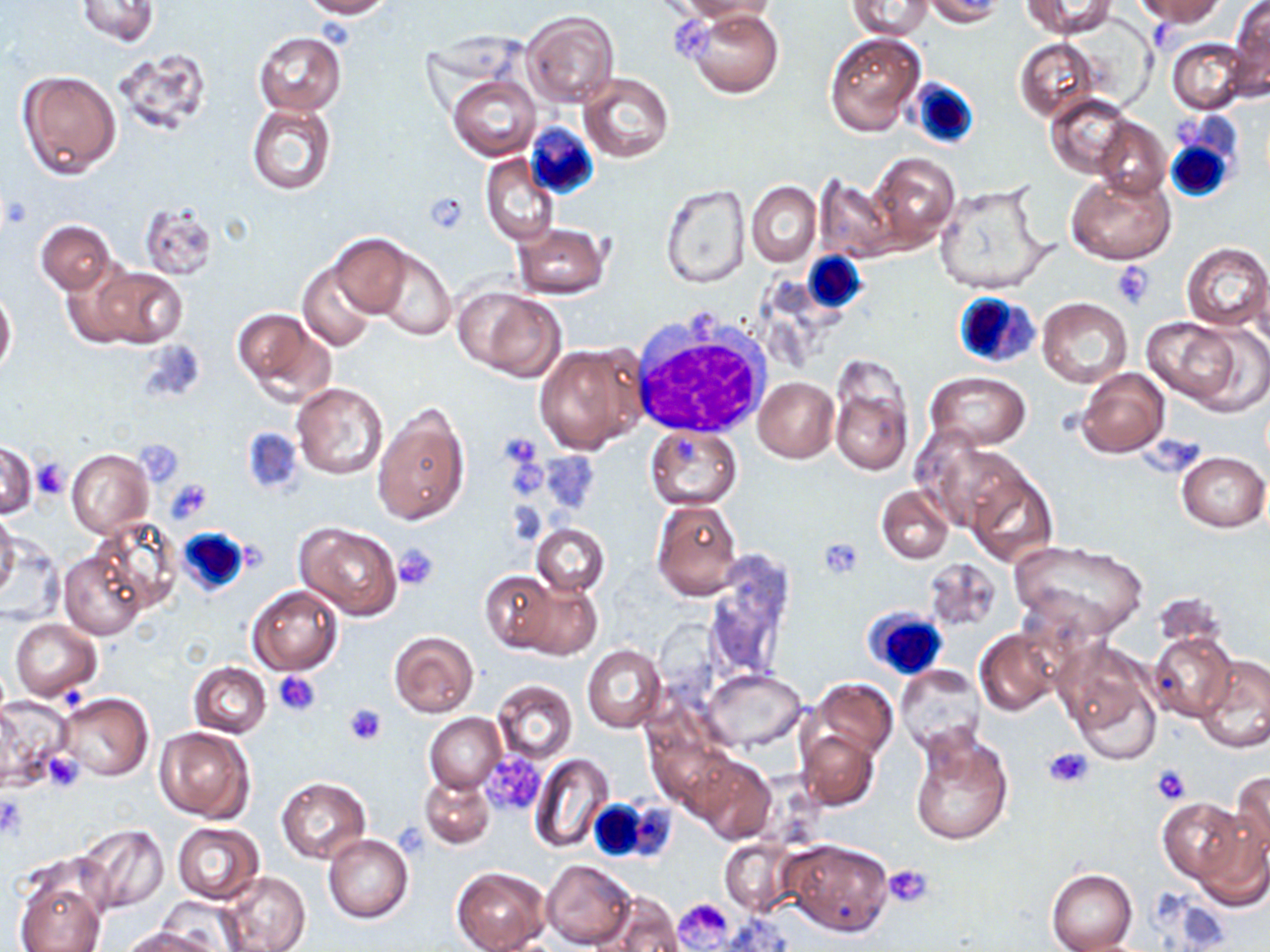 Approximate bounding boxes as named x1/y1/x2/y2 corners in pixels. Uninfected red blood cell locations (subset): (x1=297, y1=0, x2=392, y2=17), (x1=674, y1=0, x2=777, y2=21), (x1=846, y1=0, x2=933, y2=39), (x1=920, y1=0, x2=1008, y2=26), (x1=1023, y1=0, x2=1114, y2=37), (x1=1135, y1=0, x2=1224, y2=25), (x1=77, y1=1, x2=159, y2=46), (x1=1227, y1=1, x2=1269, y2=96), (x1=687, y1=9, x2=783, y2=98), (x1=521, y1=11, x2=619, y2=107), (x1=253, y1=31, x2=347, y2=117), (x1=824, y1=32, x2=926, y2=138), (x1=1166, y1=37, x2=1249, y2=114), (x1=1014, y1=38, x2=1098, y2=122), (x1=112, y1=50, x2=214, y2=139), (x1=18, y1=70, x2=121, y2=178), (x1=577, y1=73, x2=673, y2=163), (x1=450, y1=75, x2=540, y2=160), (x1=1045, y1=94, x2=1133, y2=178), (x1=246, y1=102, x2=336, y2=195), (x1=1093, y1=117, x2=1169, y2=201), (x1=867, y1=153, x2=959, y2=246), (x1=480, y1=154, x2=558, y2=246), (x1=1066, y1=173, x2=1174, y2=263), (x1=814, y1=178, x2=901, y2=261), (x1=660, y1=182, x2=750, y2=287), (x1=747, y1=182, x2=821, y2=267), (x1=933, y1=182, x2=1052, y2=298), (x1=140, y1=204, x2=216, y2=280), (x1=37, y1=220, x2=113, y2=293), (x1=512, y1=223, x2=609, y2=299), (x1=330, y1=234, x2=410, y2=318), (x1=1181, y1=242, x2=1270, y2=331), (x1=375, y1=246, x2=455, y2=339), (x1=299, y1=262, x2=376, y2=351), (x1=79, y1=265, x2=187, y2=349), (x1=0, y1=286, x2=16, y2=378), (x1=461, y1=288, x2=567, y2=382), (x1=1037, y1=298, x2=1132, y2=387), (x1=232, y1=306, x2=327, y2=398), (x1=1140, y1=317, x2=1246, y2=406), (x1=533, y1=342, x2=647, y2=454), (x1=829, y1=357, x2=914, y2=476), (x1=1075, y1=368, x2=1169, y2=458), (x1=925, y1=371, x2=1031, y2=449), (x1=754, y1=376, x2=840, y2=462), (x1=292, y1=383, x2=389, y2=480), (x1=373, y1=402, x2=470, y2=525), (x1=241, y1=426, x2=303, y2=497), (x1=645, y1=426, x2=743, y2=509), (x1=918, y1=435, x2=1018, y2=529), (x1=0, y1=441, x2=37, y2=518), (x1=67, y1=449, x2=153, y2=537), (x1=1177, y1=450, x2=1269, y2=533), (x1=964, y1=466, x2=1060, y2=568), (x1=877, y1=485, x2=954, y2=564), (x1=650, y1=499, x2=742, y2=600), (x1=0, y1=511, x2=19, y2=604), (x1=90, y1=516, x2=184, y2=613), (x1=531, y1=522, x2=609, y2=596), (x1=295, y1=523, x2=401, y2=620), (x1=1009, y1=540, x2=1149, y2=645), (x1=59, y1=547, x2=148, y2=639), (x1=923, y1=558, x2=1003, y2=634), (x1=703, y1=560, x2=792, y2=685), (x1=481, y1=570, x2=559, y2=654), (x1=516, y1=581, x2=602, y2=659), (x1=247, y1=586, x2=342, y2=675), (x1=9, y1=618, x2=103, y2=700), (x1=974, y1=628, x2=1062, y2=717), (x1=389, y1=631, x2=478, y2=717), (x1=1148, y1=632, x2=1238, y2=722), (x1=1055, y1=639, x2=1165, y2=762), (x1=581, y1=644, x2=667, y2=732), (x1=1196, y1=654, x2=1270, y2=754), (x1=188, y1=663, x2=271, y2=738), (x1=895, y1=666, x2=984, y2=754), (x1=702, y1=669, x2=805, y2=750), (x1=810, y1=677, x2=898, y2=760), (x1=492, y1=679, x2=576, y2=764), (x1=56, y1=692, x2=153, y2=781), (x1=2, y1=697, x2=76, y2=784), (x1=426, y1=713, x2=504, y2=792), (x1=906, y1=724, x2=1014, y2=848), (x1=154, y1=725, x2=255, y2=822), (x1=798, y1=728, x2=878, y2=810), (x1=529, y1=752, x2=614, y2=853), (x1=690, y1=755, x2=776, y2=843), (x1=1230, y1=770, x2=1270, y2=861), (x1=420, y1=776, x2=494, y2=848), (x1=277, y1=778, x2=370, y2=863), (x1=1157, y1=797, x2=1247, y2=884), (x1=1192, y1=813, x2=1269, y2=910), (x1=171, y1=822, x2=265, y2=904), (x1=76, y1=824, x2=169, y2=914), (x1=324, y1=834, x2=413, y2=923), (x1=719, y1=838, x2=797, y2=914), (x1=781, y1=839, x2=894, y2=936), (x1=542, y1=860, x2=634, y2=948), (x1=452, y1=866, x2=551, y2=952), (x1=1047, y1=870, x2=1137, y2=951), (x1=215, y1=871, x2=310, y2=952), (x1=14, y1=876, x2=105, y2=952), (x1=601, y1=892, x2=683, y2=952), (x1=118, y1=926, x2=216, y2=952). Platelet locations (subset): (x1=424, y1=190, x2=470, y2=232), (x1=2, y1=194, x2=34, y2=230), (x1=1111, y1=262, x2=1154, y2=308), (x1=497, y1=433, x2=541, y2=469), (x1=31, y1=459, x2=70, y2=500), (x1=166, y1=480, x2=211, y2=523), (x1=818, y1=537, x2=865, y2=578), (x1=394, y1=545, x2=438, y2=590), (x1=273, y1=671, x2=320, y2=716), (x1=344, y1=704, x2=386, y2=746), (x1=1046, y1=747, x2=1095, y2=788), (x1=43, y1=752, x2=84, y2=792), (x1=478, y1=753, x2=547, y2=815), (x1=1151, y1=765, x2=1192, y2=804), (x1=0, y1=792, x2=28, y2=842), (x1=884, y1=863, x2=934, y2=908), (x1=675, y1=897, x2=733, y2=948). White blood cell locations: (x1=908, y1=77, x2=979, y2=149), (x1=526, y1=123, x2=598, y2=198), (x1=1165, y1=132, x2=1237, y2=203), (x1=803, y1=252, x2=868, y2=313), (x1=952, y1=291, x2=1041, y2=373), (x1=630, y1=314, x2=772, y2=439), (x1=175, y1=527, x2=249, y2=595), (x1=863, y1=605, x2=948, y2=681), (x1=587, y1=797, x2=647, y2=863). Slide-level diagnosis: no evidence of blood parasites. One field of a larger specimen. 1000x magnification. May-Grünwald-Giemsa stain. Image is 1270×952 pixels. Optical microscopy. Thin blood film.